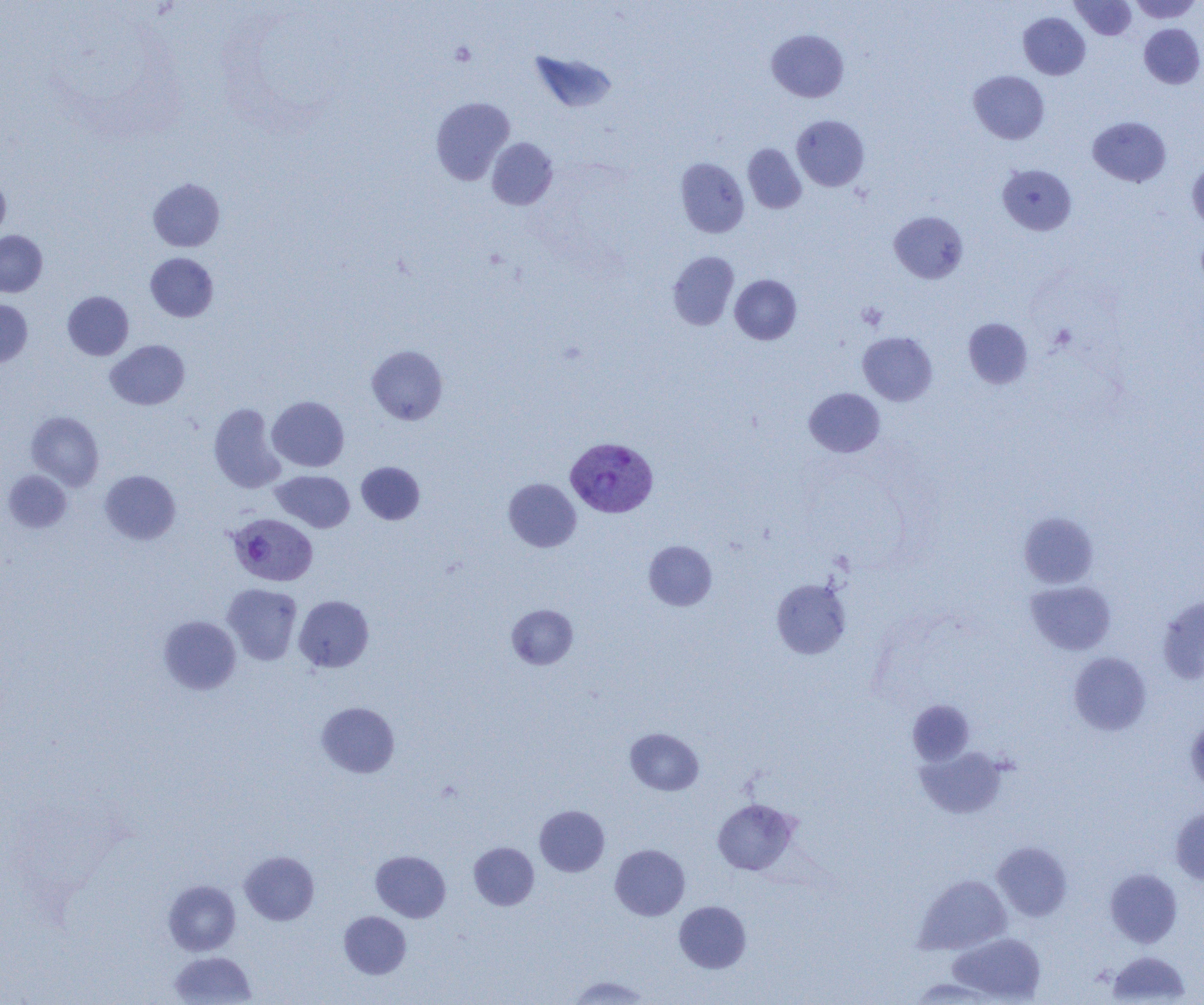
{
  "slide_level_diagnosis": "Plasmodium vivax",
  "image_size": "1204×1005 pixels",
  "plasmodium_vivax_infected_red_blood_cell_locations": "approximate bounding boxes as named x1/y1/x2/y2 corners in pixels: (x1=568, y1=439, x2=661, y2=520), (x1=227, y1=513, x2=318, y2=586)",
  "preparation": "thin blood smear",
  "uninfected_red_blood_cell_locations": "approximate bounding boxes as named x1/y1/x2/y2 corners in pixels: (x1=1129, y1=0, x2=1202, y2=23), (x1=1071, y1=1, x2=1136, y2=39), (x1=1019, y1=13, x2=1090, y2=79), (x1=1139, y1=24, x2=1204, y2=89), (x1=767, y1=29, x2=848, y2=102), (x1=530, y1=51, x2=617, y2=114), (x1=968, y1=70, x2=1049, y2=144), (x1=430, y1=96, x2=515, y2=185), (x1=792, y1=115, x2=869, y2=191), (x1=1088, y1=117, x2=1171, y2=187), (x1=487, y1=138, x2=558, y2=210), (x1=743, y1=144, x2=806, y2=213), (x1=675, y1=158, x2=749, y2=238), (x1=1187, y1=160, x2=1204, y2=231), (x1=998, y1=164, x2=1076, y2=235), (x1=0, y1=172, x2=11, y2=242), (x1=148, y1=178, x2=225, y2=251), (x1=889, y1=212, x2=968, y2=283), (x1=0, y1=230, x2=47, y2=297), (x1=668, y1=251, x2=739, y2=330), (x1=145, y1=253, x2=218, y2=322), (x1=730, y1=274, x2=801, y2=344), (x1=62, y1=291, x2=134, y2=360), (x1=0, y1=298, x2=32, y2=368), (x1=963, y1=318, x2=1033, y2=389), (x1=858, y1=331, x2=937, y2=405), (x1=106, y1=340, x2=190, y2=410), (x1=367, y1=345, x2=448, y2=425), (x1=804, y1=388, x2=885, y2=457), (x1=267, y1=396, x2=349, y2=472), (x1=208, y1=403, x2=286, y2=493), (x1=26, y1=411, x2=104, y2=490), (x1=356, y1=461, x2=425, y2=525), (x1=2, y1=470, x2=72, y2=533), (x1=100, y1=470, x2=181, y2=544), (x1=271, y1=470, x2=355, y2=532), (x1=503, y1=478, x2=581, y2=552), (x1=1018, y1=512, x2=1098, y2=589), (x1=643, y1=540, x2=717, y2=610), (x1=771, y1=577, x2=851, y2=659), (x1=1025, y1=580, x2=1116, y2=655), (x1=223, y1=583, x2=302, y2=664), (x1=294, y1=595, x2=374, y2=672), (x1=1157, y1=595, x2=1204, y2=685), (x1=506, y1=604, x2=578, y2=670), (x1=158, y1=616, x2=241, y2=694), (x1=1068, y1=652, x2=1151, y2=736), (x1=907, y1=699, x2=975, y2=765), (x1=316, y1=702, x2=399, y2=778), (x1=1185, y1=716, x2=1204, y2=795), (x1=625, y1=728, x2=704, y2=795), (x1=914, y1=746, x2=1007, y2=819), (x1=713, y1=798, x2=798, y2=875), (x1=535, y1=805, x2=609, y2=876), (x1=1170, y1=807, x2=1204, y2=885), (x1=469, y1=842, x2=539, y2=910), (x1=993, y1=842, x2=1072, y2=921), (x1=610, y1=844, x2=690, y2=920), (x1=240, y1=850, x2=319, y2=925), (x1=371, y1=850, x2=451, y2=922), (x1=1105, y1=868, x2=1182, y2=947), (x1=914, y1=875, x2=1011, y2=954), (x1=164, y1=879, x2=241, y2=956), (x1=674, y1=901, x2=751, y2=972), (x1=339, y1=911, x2=411, y2=979), (x1=948, y1=932, x2=1045, y2=1003), (x1=169, y1=951, x2=257, y2=1005), (x1=1107, y1=951, x2=1191, y2=1004), (x1=565, y1=975, x2=650, y2=1005), (x1=908, y1=978, x2=1001, y2=1004)",
  "platelet_locations": "approximate bounding boxes as named x1/y1/x2/y2 corners in pixels: (x1=449, y1=42, x2=476, y2=66), (x1=857, y1=302, x2=888, y2=330), (x1=1049, y1=323, x2=1076, y2=351)",
  "magnification": "1000x",
  "modality": "optical microscopy",
  "field_of_view": "one of a larger specimen"
}